Locate every malaria parasite and identify its life-cycle stage.
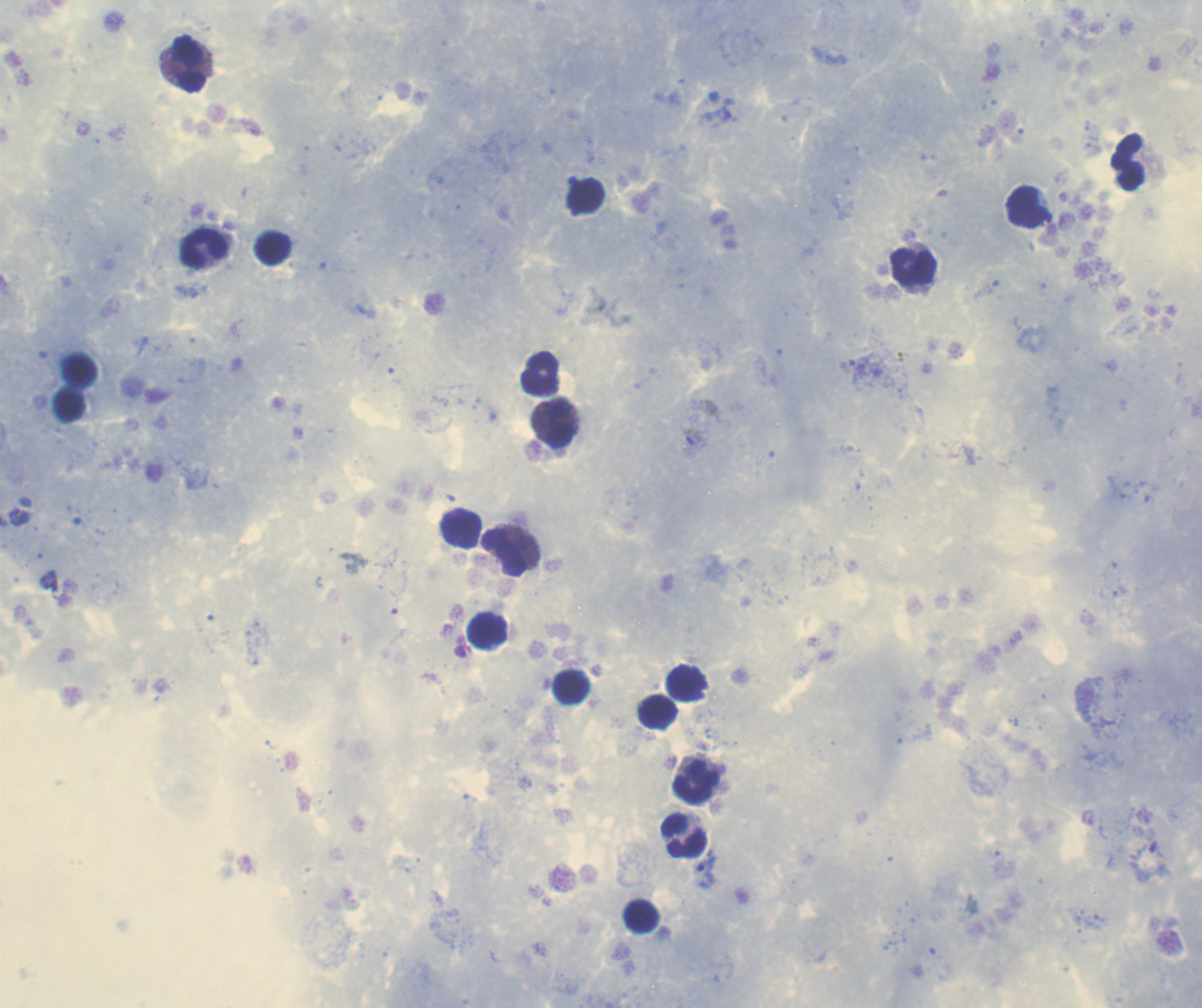

Approximate object centers, in pixels from the top-left corner.
Trophozoites: (x=21, y=517), (x=707, y=872).
Gametocytes: (x=693, y=437).
No schizont forms observed.

coordinate format = approximate object centers, in pixels from the top-left corner
leukocyte locations = (x=189, y=63), (x=1129, y=162), (x=1028, y=208), (x=204, y=249), (x=272, y=249), (x=913, y=268), (x=540, y=373), (x=557, y=424), (x=461, y=529), (x=504, y=553), (x=487, y=631), (x=686, y=681), (x=571, y=687), (x=658, y=712), (x=696, y=782), (x=684, y=834), (x=642, y=917)
image size = 1202×1008 pixels
stain = Romanowsky
coloration quality = good
magnification = 100x
preparation = thick blood smear
context = previously used in a real diagnosis
background quality = good
field of view = single